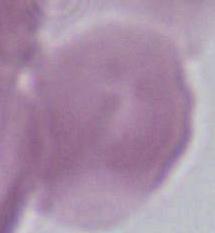

magnification: 1000x
identification: red blood cell
modality: photomicrograph